Name the parasite shown.
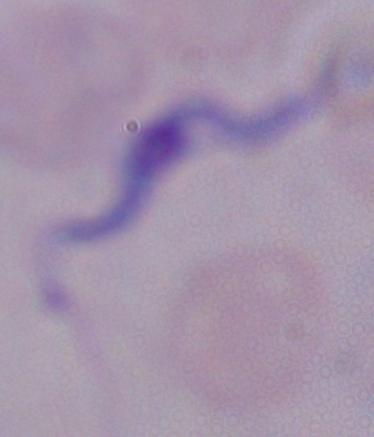
This is a trypanosome.

modality: micrograph
magnification: 1000x